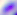

identification = Toxoplasma gondii
modality = photomicrograph
magnification = 400x